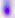
{
  "magnification": "400x",
  "identification": "Toxoplasma gondii",
  "modality": "photomicrograph"
}